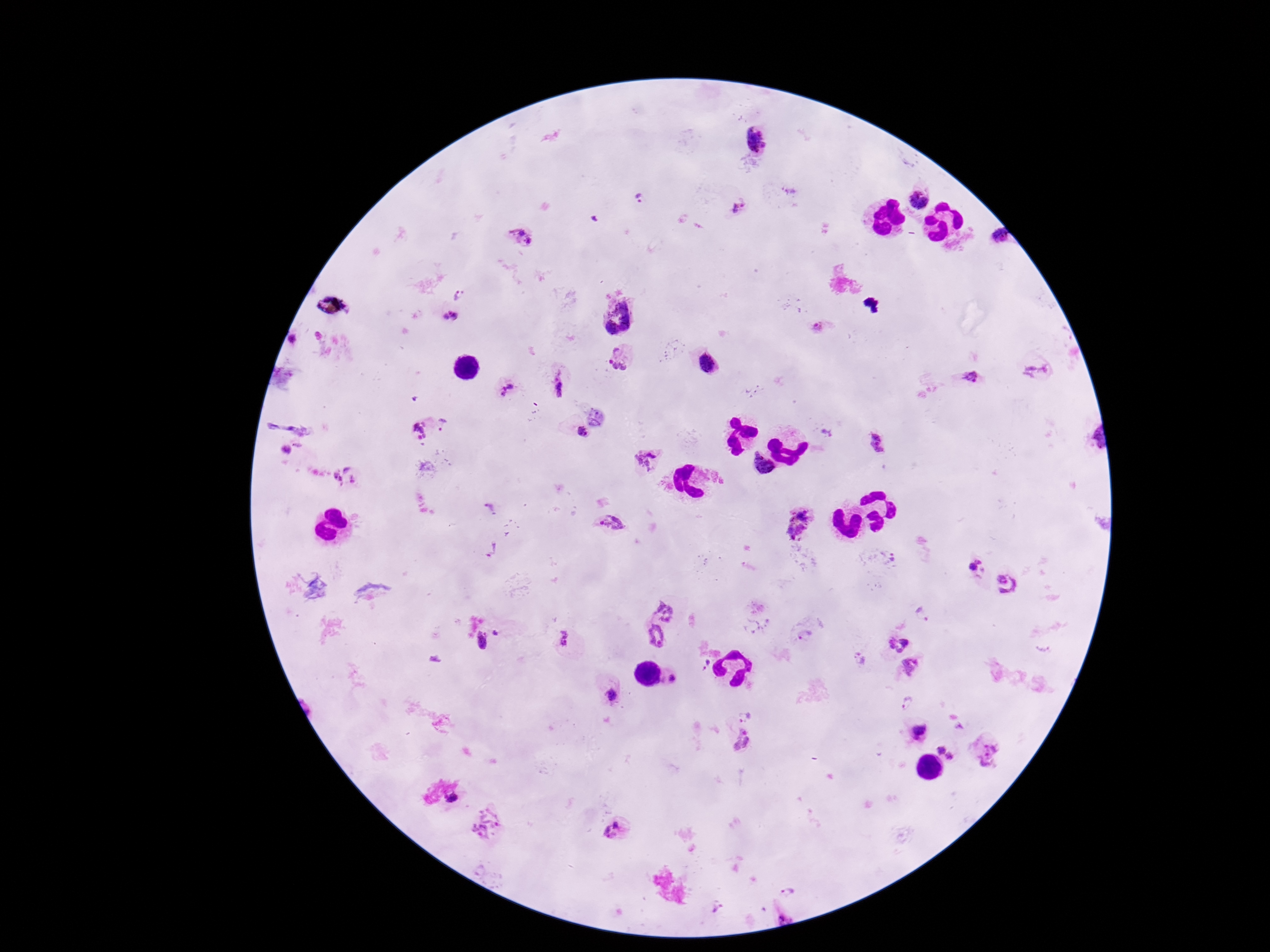
magnification = 100x
stain = Giemsa
image size = 1270×952 pixels
Plasmodium parasite locations = approximate object centers, in pixels from the top-left corner: (x=753, y=141), (x=791, y=193), (x=919, y=198), (x=639, y=201), (x=737, y=211), (x=524, y=236), (x=997, y=240), (x=464, y=295), (x=448, y=318), (x=621, y=355), (x=1035, y=370), (x=974, y=378), (x=504, y=387), (x=558, y=387), (x=443, y=428), (x=421, y=430), (x=827, y=433), (x=583, y=435), (x=876, y=443), (x=651, y=460), (x=343, y=477), (x=489, y=508), (x=611, y=522), (x=798, y=522), (x=491, y=549), (x=892, y=555), (x=975, y=568), (x=1009, y=584), (x=665, y=608), (x=920, y=615), (x=755, y=624), (x=497, y=631), (x=805, y=636), (x=657, y=637), (x=563, y=639), (x=482, y=640), (x=897, y=642), (x=858, y=660), (x=703, y=663), (x=912, y=666), (x=673, y=679), (x=611, y=695), (x=907, y=703), (x=744, y=712), (x=916, y=730), (x=743, y=741), (x=940, y=748), (x=991, y=751), (x=950, y=756), (x=450, y=799), (x=486, y=824), (x=611, y=829), (x=787, y=890)
preparation = thick blood film
capture = smartphone camera through the microscope eyepiece
field of view = single
patient malaria status = positive